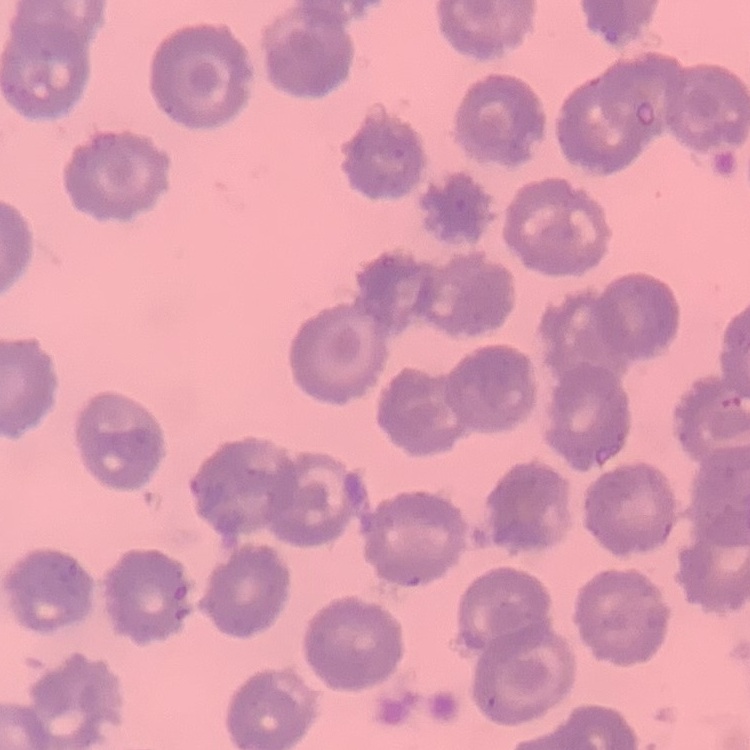

{
  "erythrocyte_morphology": "no rouleaux formation",
  "image_type": "one tile cut from a larger photomicrograph",
  "preparation": "thin blood film",
  "stain": "Field's or Giemsa"
}